Locate every blood parasite and identify its species.
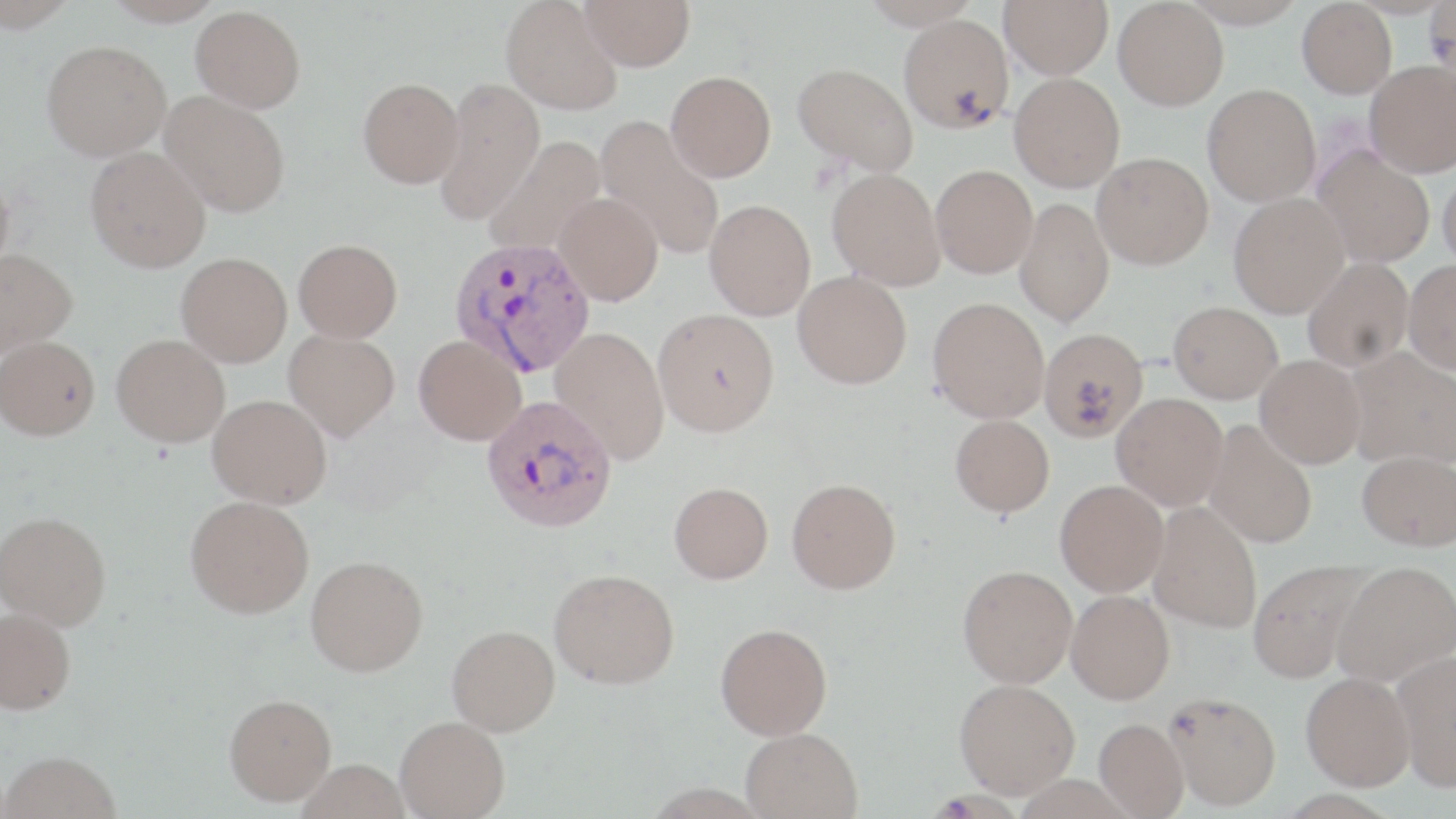
Approximate bounding boxes as (x1, y1, x2, y2) in pixels.
Plasmodium vivax-infected red blood cells: (449, 237, 594, 377), (482, 395, 618, 533).
No Plasmodium falciparum, Plasmodium ovale, Plasmodium malariae, Babesia divergens, or Trypanosoma brucei observed.

Summary:
  - Uninfected red blood cell locations: (0, 0, 79, 32), (102, 0, 225, 26), (502, 0, 623, 115), (579, 0, 695, 71), (999, 0, 1113, 78), (1113, 0, 1229, 110), (1182, 1, 1306, 27), (1297, 1, 1397, 98), (1426, 3, 1456, 82), (191, 5, 306, 113), (898, 14, 1014, 133), (41, 40, 171, 160), (1365, 60, 1456, 178), (793, 63, 918, 175), (666, 71, 776, 182), (1009, 73, 1125, 192), (434, 76, 545, 223), (358, 77, 464, 187), (1203, 83, 1320, 206), (160, 91, 291, 217), (595, 115, 726, 260), (485, 137, 607, 257), (85, 146, 210, 272), (1313, 147, 1435, 267), (1092, 152, 1213, 269), (930, 164, 1038, 278), (1437, 165, 1456, 272), (0, 167, 14, 280), (828, 168, 945, 290), (554, 192, 663, 306), (1229, 193, 1349, 318), (1015, 198, 1114, 327), (704, 200, 815, 320), (294, 238, 402, 342), (0, 247, 77, 358), (176, 252, 292, 367), (1302, 257, 1413, 372), (1403, 259, 1456, 373), (793, 271, 912, 389), (928, 297, 1050, 422), (1168, 301, 1283, 403), (653, 308, 780, 437), (550, 326, 670, 463), (1039, 326, 1148, 441), (284, 330, 400, 441), (111, 334, 230, 446), (0, 335, 100, 440), (413, 335, 526, 445), (1346, 347, 1456, 469), (1255, 354, 1367, 469), (1111, 393, 1228, 510), (208, 394, 332, 508), (950, 414, 1054, 516), (1203, 420, 1317, 549), (1356, 450, 1456, 550), (786, 478, 901, 593), (1055, 479, 1169, 596), (669, 481, 774, 584), (185, 495, 314, 618), (1148, 501, 1263, 633), (1, 511, 111, 629), (305, 555, 428, 676), (1248, 559, 1374, 683), (1333, 561, 1456, 685), (958, 564, 1078, 687), (549, 568, 679, 689), (1066, 589, 1175, 704), (0, 607, 76, 714), (716, 623, 833, 739), (447, 625, 560, 735), (1391, 650, 1456, 791), (1301, 672, 1415, 790), (954, 678, 1079, 798), (1165, 692, 1281, 810), (225, 693, 337, 805), (395, 716, 510, 818), (1094, 717, 1189, 818), (741, 727, 863, 818), (0, 750, 122, 819), (296, 759, 410, 819)
  - Slide-level diagnosis: Plasmodium vivax
  - Field of view: single
  - Magnification: 1000x
  - Preparation: thin blood film
  - Modality: light microscopy
  - Image size: 1456×819 pixels
  - Stain: May-Grünwald-Giemsa